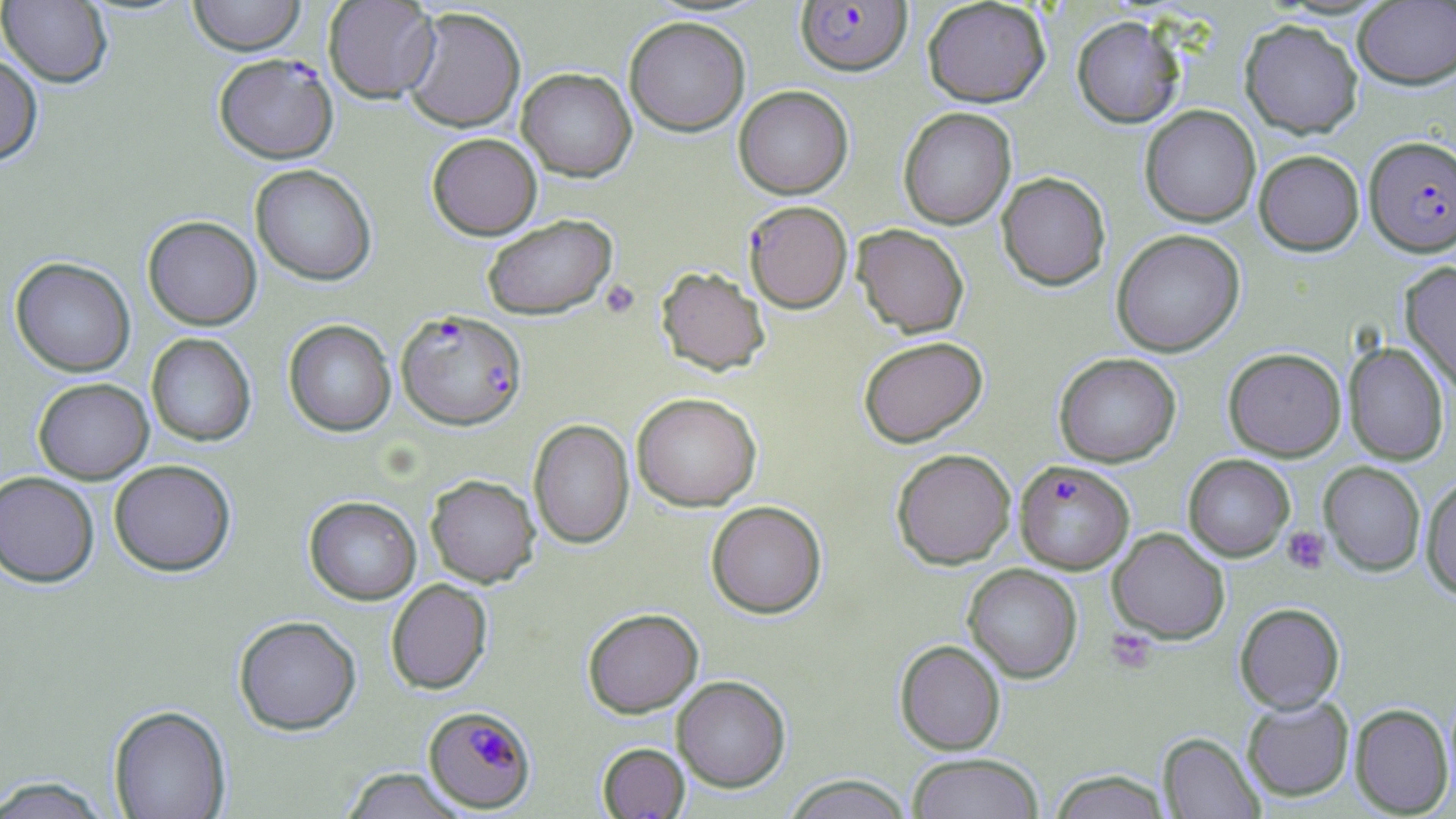

Approximate bounding boxes as (x1,y1)-(x2,y2) corner pairs in pixels. Uninfected red blood cell locations: (0,0)-(113,88), (187,0)-(306,55), (323,0)-(439,103), (922,0)-(1051,107), (1353,2)-(1456,89), (402,7)-(526,133), (1071,15)-(1185,128), (624,16)-(750,136), (1240,19)-(1363,138), (0,54)-(43,166), (517,68)-(636,181), (733,85)-(854,199), (1139,105)-(1260,227), (898,107)-(1017,229), (427,133)-(542,239), (1254,150)-(1365,255), (250,164)-(377,286), (997,172)-(1111,290), (482,213)-(617,319), (143,215)-(262,330), (853,224)-(969,337), (1111,229)-(1245,356), (10,257)-(135,377), (1400,262)-(1456,396), (656,266)-(770,376), (283,319)-(396,436), (146,333)-(256,447), (858,336)-(988,447), (1343,341)-(1449,465), (1223,347)-(1346,461), (1054,353)-(1181,467), (33,378)-(154,484), (631,392)-(762,511), (529,419)-(635,549), (891,448)-(1016,569), (1183,454)-(1295,561), (109,459)-(237,577), (1319,462)-(1426,575), (0,471)-(99,588), (425,474)-(540,587), (1421,475)-(1456,600), (304,495)-(421,604), (706,500)-(827,618), (1108,527)-(1230,644), (963,563)-(1082,683), (386,578)-(493,695), (1235,602)-(1345,713), (583,607)-(703,717), (234,614)-(362,734), (894,639)-(1005,754), (672,675)-(791,792), (1242,695)-(1354,801), (1349,703)-(1453,816), (108,704)-(232,819), (1158,732)-(1264,819), (597,743)-(690,818), (906,753)-(1045,819), (339,768)-(468,818), (1047,770)-(1173,819), (0,775)-(114,818), (783,775)-(914,818). Platelet locations: (600,279)-(640,319), (1283,526)-(1331,574), (1106,629)-(1156,673). Plasmodium falciparum-infected red blood cell locations: (795,1)-(912,75), (214,53)-(339,164), (1365,135)-(1456,257), (748,200)-(856,313), (396,309)-(527,430), (1015,460)-(1134,574), (423,705)-(537,813). Slide-level diagnosis: Plasmodium falciparum. May-Grünwald-Giemsa-stained preparation. Single field of view. Light microscopy. Image is 1456×819 pixels. Thin blood smear. Captured at 1000x magnification.